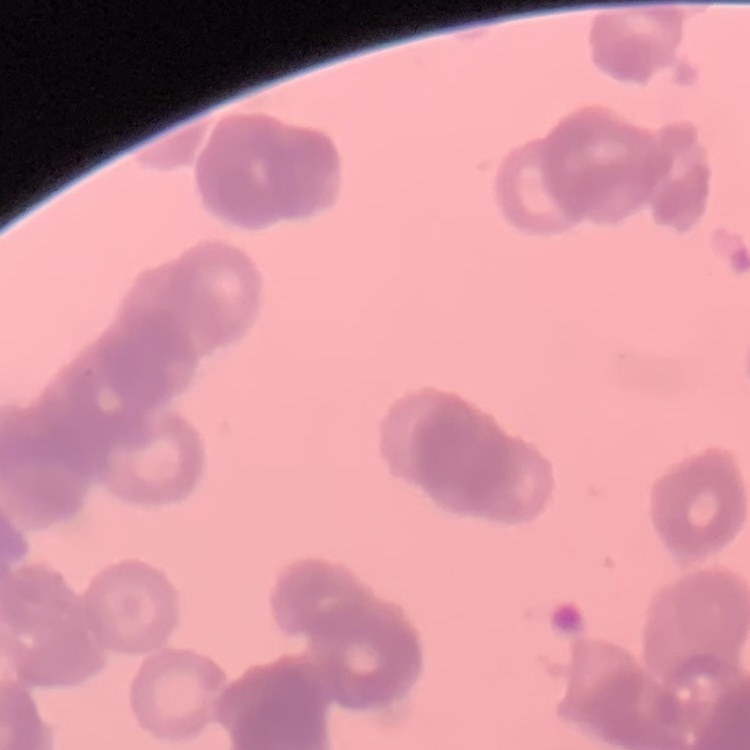
red blood cell morphology = rouleaux formation
stain = Field's or Giemsa
image type = one tile cut from a larger photomicrograph
preparation = thin blood film